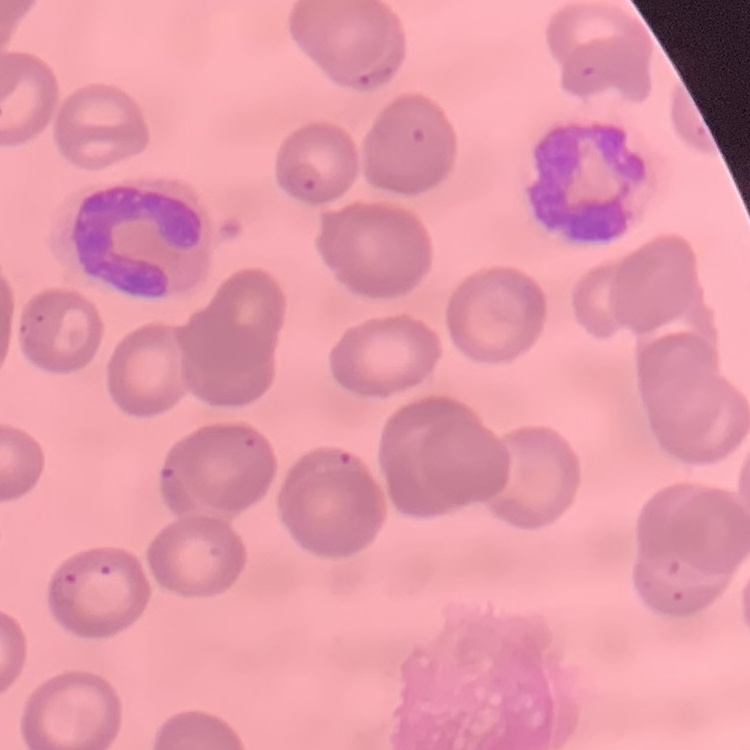

Summary:
  - Red blood cell morphology: no rouleaux formation
  - Stain: Field's or Giemsa
  - Preparation: thin peripheral smear
  - Image type: one tile cut from a larger photomicrograph